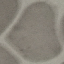 Result: no malaria parasites seen. Automatically extracted cell patch, resized to 64 × 64 pixels. Thin blood film. Giemsa-stained preparation. Acquired by smartphone through the microscope eyepiece.